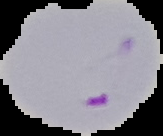 Image is 163×136 pixels. From a thin blood smear. Result: malaria parasites identified. The area outside the segmented cell region is set to black.